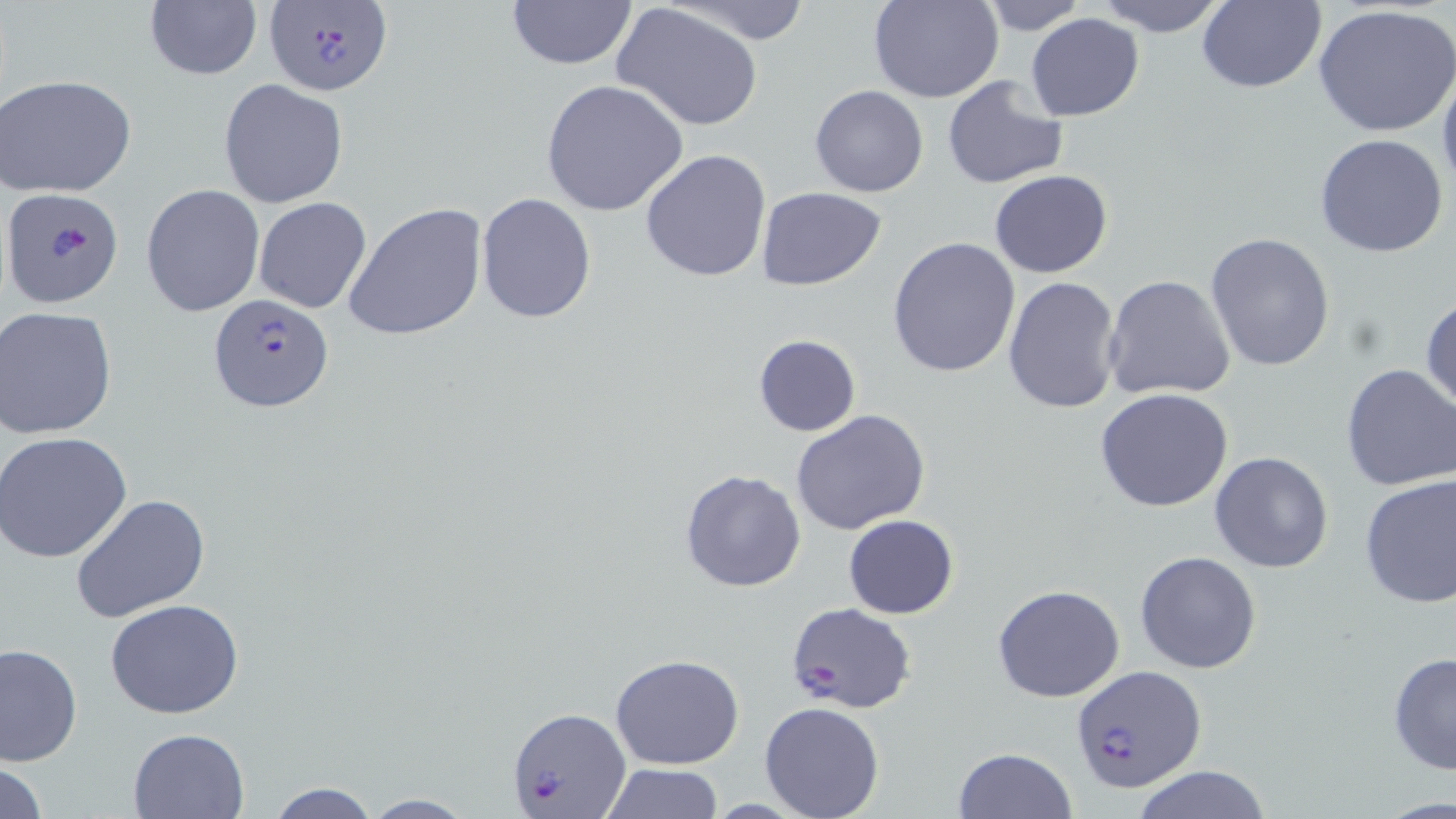 Approximate bounding boxes as [x1, y1, x2, y2] in pixels. Uninfected red blood cell locations: [663, 0, 819, 46], [868, 0, 1004, 103], [1090, 0, 1230, 35], [505, 1, 637, 71], [977, 1, 1091, 35], [1194, 1, 1326, 93], [143, 2, 263, 81], [611, 4, 767, 132], [1313, 4, 1456, 139], [1027, 14, 1144, 121], [1437, 65, 1456, 205], [2, 73, 137, 197], [942, 73, 1069, 190], [218, 79, 348, 207], [541, 80, 689, 218], [809, 85, 930, 198], [1314, 133, 1451, 259], [640, 148, 771, 284], [989, 170, 1113, 277], [141, 184, 266, 319], [757, 186, 886, 290], [476, 192, 597, 324], [253, 197, 372, 314], [343, 202, 488, 342], [1205, 233, 1335, 374], [888, 236, 1022, 378], [1001, 275, 1122, 416], [1103, 275, 1236, 403], [1420, 292, 1455, 417], [1, 306, 118, 439], [752, 334, 861, 437], [1339, 362, 1456, 492], [1095, 387, 1236, 514], [790, 410, 933, 535], [1, 431, 133, 561], [1208, 452, 1334, 574], [680, 468, 806, 594], [1358, 474, 1456, 608], [69, 494, 212, 625], [842, 514, 959, 619], [1134, 551, 1262, 674], [992, 584, 1125, 703], [104, 599, 245, 719], [1, 643, 82, 765], [1386, 650, 1456, 776], [610, 654, 744, 770], [759, 701, 885, 819], [128, 727, 249, 817], [953, 747, 1077, 819], [0, 759, 49, 818], [600, 762, 724, 817], [1130, 766, 1272, 819], [263, 780, 382, 817], [358, 794, 478, 817]. Plasmodium falciparum-infected red blood cell locations: [266, 0, 394, 95], [4, 186, 124, 309], [209, 295, 334, 414], [787, 603, 915, 712], [1070, 666, 1207, 794], [509, 706, 630, 818]. Slide-level diagnosis: Plasmodium falciparum. Captured at 1000x magnification. Image is 1456×819 pixels. One field of a larger specimen. Thin blood film. Optical microscopy. May-Grünwald-Giemsa stain.